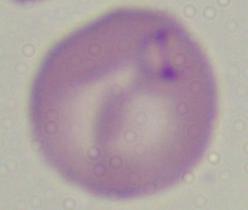

identification = Babesia
magnification = 1000x
modality = micrograph